Locate every white blood cell.
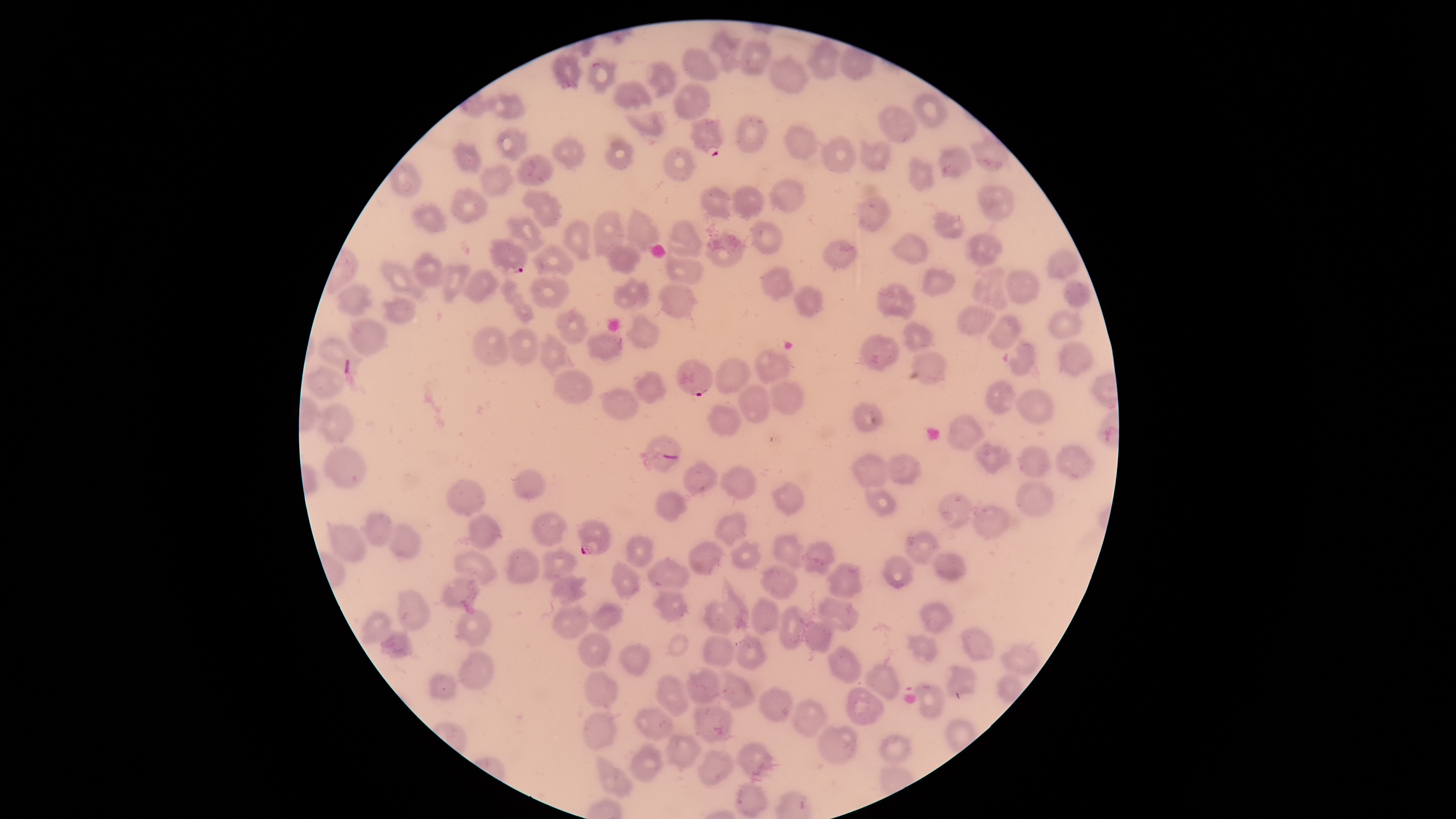

No white blood cells identified.

Approximate bounding boxes, in pixels from the top-left corner.
Summary:
  - Parasitized red blood cells: (left=690, top=117, right=723, bottom=156), (left=488, top=237, right=529, bottom=276), (left=676, top=358, right=714, bottom=396), (left=576, top=519, right=612, bottom=556)
  - Uninfected red blood cells: (left=706, top=28, right=742, bottom=74), (left=738, top=38, right=772, bottom=76), (left=805, top=38, right=841, bottom=80), (left=682, top=47, right=720, bottom=82), (left=549, top=52, right=585, bottom=90), (left=767, top=54, right=809, bottom=94), (left=584, top=56, right=619, bottom=93), (left=644, top=61, right=679, bottom=99), (left=611, top=78, right=654, bottom=111), (left=671, top=82, right=712, bottom=120), (left=488, top=93, right=527, bottom=120), (left=913, top=93, right=948, bottom=129), (left=876, top=104, right=918, bottom=145), (left=623, top=109, right=668, bottom=137), (left=735, top=112, right=770, bottom=153), (left=782, top=124, right=818, bottom=160), (left=494, top=125, right=529, bottom=162), (left=969, top=132, right=1010, bottom=172), (left=818, top=135, right=856, bottom=173), (left=550, top=136, right=587, bottom=170), (left=603, top=136, right=636, bottom=170), (left=858, top=138, right=893, bottom=172), (left=450, top=140, right=482, bottom=177), (left=937, top=144, right=973, bottom=177), (left=662, top=145, right=698, bottom=183), (left=515, top=154, right=555, bottom=187), (left=907, top=155, right=935, bottom=192), (left=387, top=159, right=424, bottom=197), (left=479, top=164, right=515, bottom=197), (left=769, top=179, right=807, bottom=213), (left=731, top=184, right=765, bottom=221), (left=977, top=184, right=1016, bottom=222), (left=450, top=186, right=490, bottom=224), (left=699, top=186, right=732, bottom=221), (left=521, top=189, right=563, bottom=229), (left=855, top=195, right=893, bottom=234), (left=410, top=201, right=447, bottom=234), (left=622, top=205, right=661, bottom=252), (left=593, top=210, right=625, bottom=256), (left=932, top=211, right=965, bottom=239), (left=503, top=216, right=546, bottom=253), (left=562, top=219, right=592, bottom=262), (left=666, top=220, right=703, bottom=258), (left=750, top=220, right=784, bottom=256), (left=888, top=231, right=929, bottom=264), (left=964, top=231, right=1003, bottom=266), (left=703, top=232, right=747, bottom=268), (left=821, top=237, right=860, bottom=268), (left=604, top=240, right=641, bottom=275), (left=530, top=243, right=575, bottom=277), (left=664, top=249, right=705, bottom=286), (left=1046, top=249, right=1083, bottom=279), (left=411, top=252, right=444, bottom=287), (left=379, top=260, right=427, bottom=303), (left=440, top=263, right=472, bottom=303), (left=760, top=266, right=794, bottom=302), (left=919, top=266, right=956, bottom=298), (left=971, top=266, right=1010, bottom=311), (left=1004, top=268, right=1040, bottom=305), (left=461, top=269, right=500, bottom=304), (left=528, top=274, right=571, bottom=309), (left=612, top=274, right=650, bottom=311), (left=497, top=277, right=535, bottom=325), (left=1062, top=281, right=1092, bottom=308), (left=656, top=282, right=700, bottom=319), (left=335, top=283, right=374, bottom=317), (left=875, top=283, right=916, bottom=319), (left=792, top=286, right=824, bottom=318), (left=381, top=294, right=418, bottom=325), (left=956, top=305, right=996, bottom=337), (left=555, top=308, right=590, bottom=346), (left=1047, top=308, right=1083, bottom=339), (left=624, top=314, right=661, bottom=349), (left=985, top=314, right=1022, bottom=349), (left=348, top=318, right=390, bottom=356), (left=900, top=319, right=935, bottom=353), (left=470, top=325, right=509, bottom=366), (left=506, top=326, right=539, bottom=368), (left=538, top=331, right=568, bottom=373), (left=585, top=331, right=623, bottom=364), (left=859, top=334, right=901, bottom=372), (left=316, top=337, right=364, bottom=379), (left=1001, top=339, right=1036, bottom=377), (left=1057, top=341, right=1094, bottom=377), (left=755, top=347, right=792, bottom=384), (left=909, top=351, right=947, bottom=386), (left=714, top=356, right=751, bottom=395), (left=304, top=365, right=346, bottom=399), (left=553, top=368, right=594, bottom=404), (left=632, top=370, right=667, bottom=404), (left=985, top=380, right=1017, bottom=415), (left=768, top=381, right=804, bottom=416), (left=737, top=384, right=770, bottom=424), (left=597, top=387, right=641, bottom=420), (left=1015, top=388, right=1055, bottom=425), (left=851, top=401, right=885, bottom=433), (left=316, top=402, right=356, bottom=444), (left=706, top=402, right=742, bottom=437), (left=946, top=413, right=986, bottom=454), (left=640, top=433, right=682, bottom=473), (left=972, top=439, right=1012, bottom=476), (left=1054, top=443, right=1096, bottom=480), (left=322, top=445, right=369, bottom=489), (left=1018, top=445, right=1053, bottom=478), (left=849, top=452, right=890, bottom=490), (left=884, top=452, right=924, bottom=486), (left=682, top=460, right=720, bottom=497), (left=718, top=465, right=758, bottom=501), (left=512, top=468, right=547, bottom=500), (left=444, top=479, right=487, bottom=518), (left=770, top=480, right=805, bottom=516), (left=1015, top=480, right=1055, bottom=517), (left=865, top=489, right=897, bottom=518), (left=654, top=490, right=688, bottom=523), (left=937, top=492, right=973, bottom=528), (left=971, top=504, right=1010, bottom=542), (left=360, top=510, right=396, bottom=546), (left=714, top=510, right=748, bottom=548), (left=531, top=511, right=569, bottom=547), (left=467, top=513, right=503, bottom=551), (left=326, top=521, right=368, bottom=563), (left=386, top=523, right=422, bottom=560), (left=903, top=529, right=941, bottom=566), (left=771, top=532, right=806, bottom=572), (left=624, top=536, right=655, bottom=568), (left=688, top=541, right=725, bottom=576), (left=730, top=541, right=762, bottom=570), (left=801, top=541, right=837, bottom=577), (left=541, top=545, right=578, bottom=582), (left=503, top=547, right=541, bottom=586), (left=452, top=550, right=499, bottom=587), (left=930, top=552, right=968, bottom=581), (left=881, top=554, right=914, bottom=589), (left=647, top=556, right=690, bottom=590), (left=610, top=559, right=642, bottom=600), (left=825, top=562, right=864, bottom=600), (left=759, top=564, right=798, bottom=600), (left=549, top=574, right=588, bottom=606), (left=439, top=575, right=481, bottom=615), (left=395, top=589, right=433, bottom=632), (left=651, top=590, right=688, bottom=622), (left=817, top=595, right=861, bottom=632), (left=750, top=597, right=781, bottom=636), (left=702, top=599, right=741, bottom=635), (left=918, top=600, right=955, bottom=635), (left=590, top=602, right=624, bottom=632), (left=551, top=604, right=590, bottom=641), (left=778, top=605, right=809, bottom=650), (left=454, top=608, right=494, bottom=648), (left=359, top=610, right=393, bottom=644), (left=801, top=621, right=834, bottom=654), (left=958, top=625, right=995, bottom=661), (left=378, top=630, right=414, bottom=659), (left=577, top=631, right=612, bottom=670), (left=905, top=633, right=939, bottom=663), (left=700, top=634, right=735, bottom=667), (left=734, top=636, right=768, bottom=670), (left=1000, top=642, right=1041, bottom=677), (left=618, top=643, right=651, bottom=676), (left=828, top=646, right=862, bottom=684), (left=457, top=649, right=494, bottom=690), (left=863, top=663, right=901, bottom=702), (left=945, top=664, right=976, bottom=698), (left=684, top=665, right=721, bottom=705), (left=721, top=669, right=756, bottom=711), (left=584, top=670, right=619, bottom=709), (left=428, top=673, right=455, bottom=701), (left=655, top=673, right=691, bottom=717), (left=912, top=681, right=947, bottom=720), (left=759, top=685, right=794, bottom=723), (left=845, top=686, right=885, bottom=726), (left=789, top=698, right=831, bottom=739), (left=691, top=705, right=737, bottom=744), (left=633, top=707, right=675, bottom=741), (left=582, top=711, right=618, bottom=751), (left=816, top=724, right=860, bottom=765), (left=665, top=734, right=703, bottom=772), (left=878, top=734, right=914, bottom=765), (left=735, top=740, right=781, bottom=782), (left=629, top=741, right=665, bottom=783), (left=697, top=749, right=734, bottom=787), (left=594, top=754, right=634, bottom=797), (left=734, top=780, right=769, bottom=819)
  - Species: Plasmodium falciparum
  - Visible region: circular
  - Field of view: single
  - Preparation: thin blood film
  - Capture: smartphone photograph through the microscope eyepiece
  - Stain: Giemsa
  - Presence: malaria parasites detected
  - Image size: 1456×819 pixels